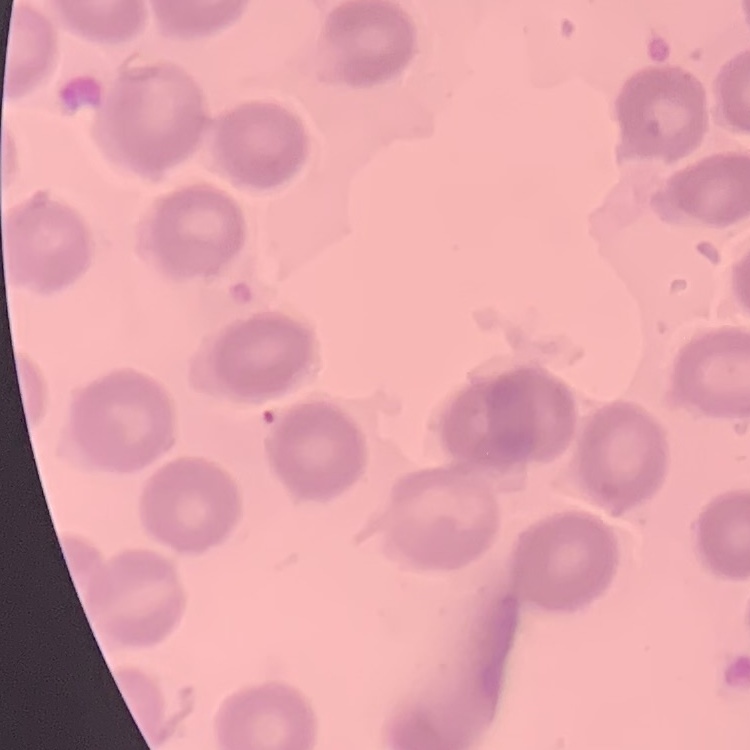
red_blood_cell_morphology: no rouleaux formation
stain: Field's or Giemsa
preparation: thin peripheral smear
image_type: square crop of a larger photomicrograph